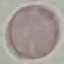

{
  "result": "negative for malaria parasites",
  "stain": "Giemsa",
  "image_type": "automatically extracted cell patch, resized to 64 × 64 pixels",
  "preparation": "thin smear",
  "capture": "smartphone through the microscope eyepiece"
}